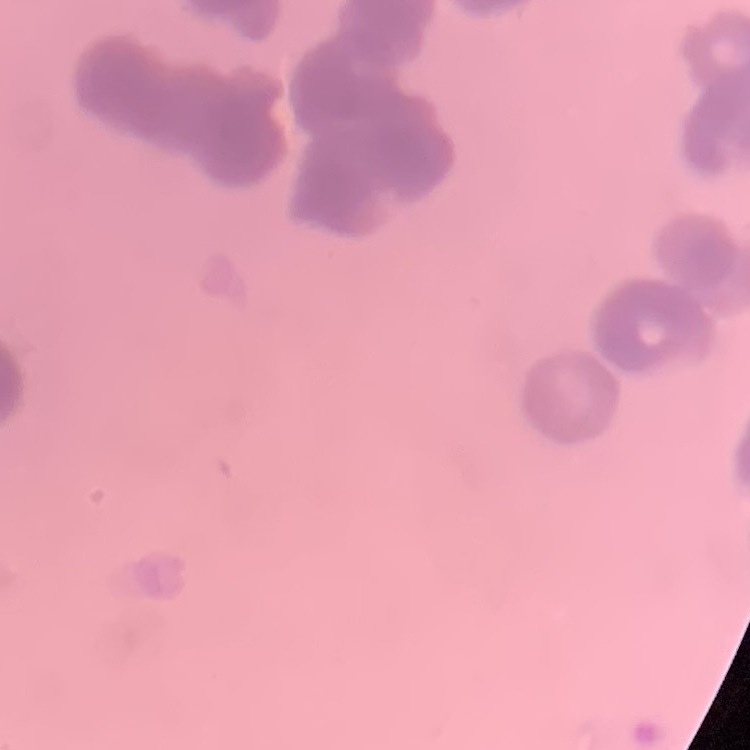

red_blood_cell_morphology: rouleaux formation
image_type: square crop of a larger photomicrograph
preparation: thin blood film
stain: Field's or Giemsa